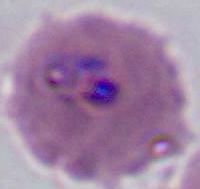
magnification: 400x or 1000x
modality: micrograph
identification: Plasmodium